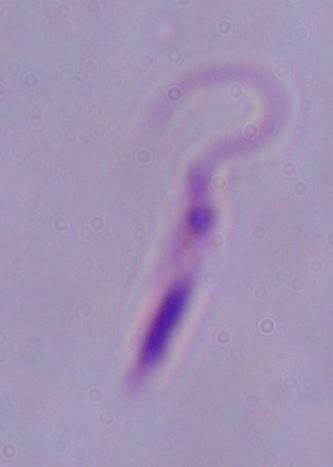
Captured at 1000x magnification. Micrograph. A Leishmania parasite is seen.